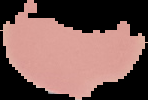

Summary:
  - Image type: cell region segmented out of the field of view; surrounding area masked to black
  - Image size: 148×100 pixels
  - Malaria status: uninfected
  - Preparation: thin blood smear